Identify the blood parasite species.
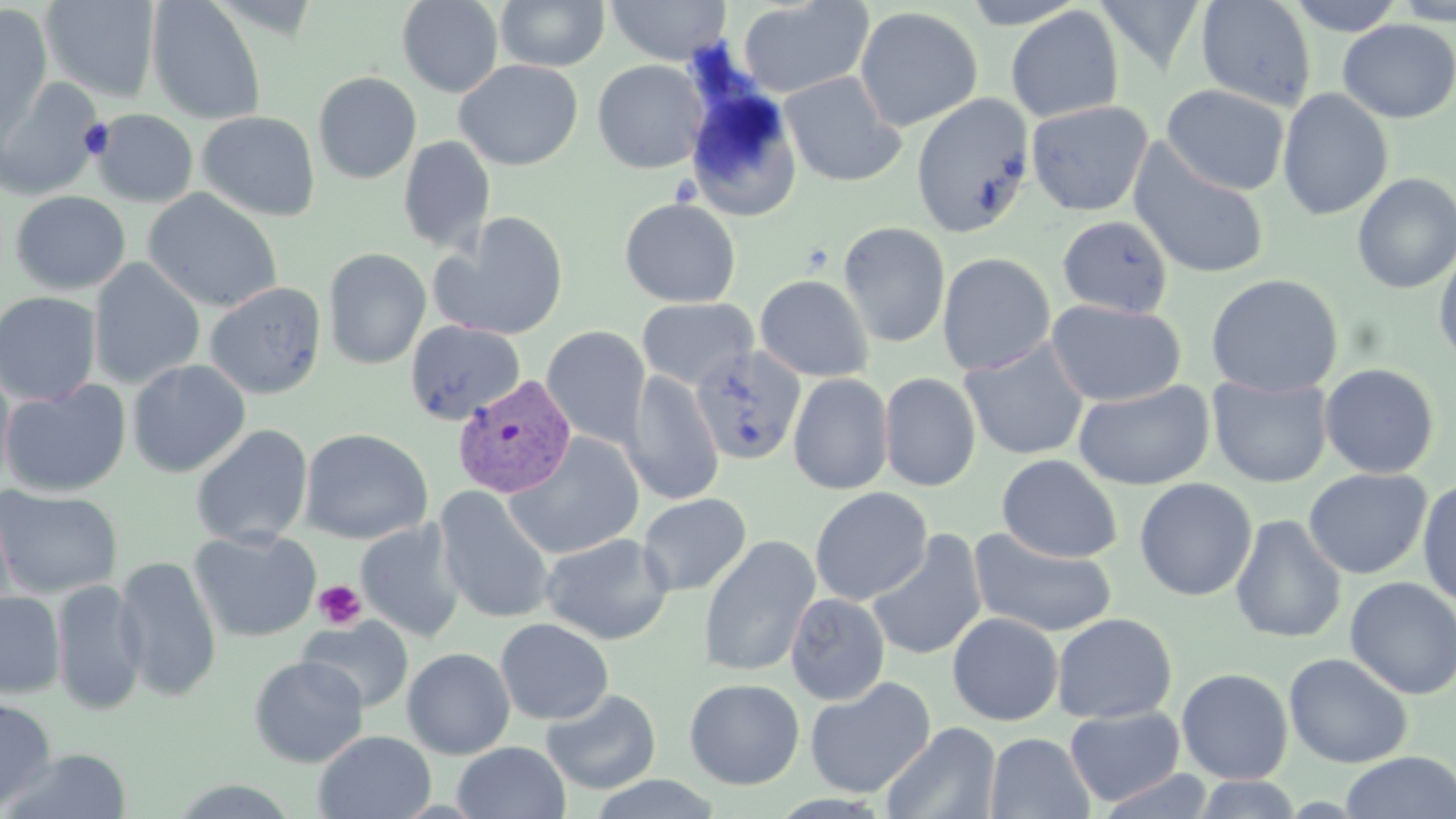

Plasmodium vivax.

preparation = thin blood smear
image size = 1456×819 pixels
uninfected red blood cell locations = approximate bounding boxes as (x1, y1, x2, y2) in pixels: (40, 0, 161, 103), (397, 0, 504, 97), (495, 0, 610, 71), (605, 0, 732, 65), (737, 0, 874, 99), (958, 0, 1088, 28), (1093, 0, 1207, 77), (1195, 0, 1317, 112), (1284, 0, 1407, 36), (1390, 0, 1456, 25), (147, 1, 266, 125), (0, 4, 53, 139), (1006, 5, 1124, 123), (854, 6, 984, 132), (1337, 19, 1456, 123), (454, 59, 583, 171), (592, 59, 708, 173), (313, 71, 422, 184), (778, 71, 907, 188), (0, 77, 104, 201), (1162, 84, 1291, 196), (1277, 88, 1394, 221), (685, 89, 803, 222), (911, 94, 1035, 238), (1026, 100, 1154, 217), (90, 109, 198, 207), (197, 111, 321, 221), (398, 136, 496, 255), (1128, 141, 1271, 280), (1352, 172, 1456, 295), (142, 188, 283, 313), (10, 191, 130, 295), (619, 198, 741, 308), (432, 212, 571, 342), (1057, 215, 1173, 318), (838, 221, 951, 348), (1433, 242, 1456, 372), (323, 248, 431, 370), (937, 252, 1056, 376), (88, 259, 205, 389), (1205, 273, 1343, 396), (754, 274, 874, 382), (204, 282, 327, 398), (0, 291, 102, 407), (637, 297, 758, 390), (1045, 299, 1186, 407), (405, 320, 525, 425), (541, 326, 651, 448), (959, 338, 1090, 462), (127, 359, 250, 478), (0, 362, 15, 489), (1319, 363, 1440, 479), (623, 372, 724, 506), (878, 372, 981, 492), (788, 373, 894, 495), (1207, 374, 1332, 488), (0, 380, 131, 498), (1073, 380, 1214, 491), (191, 424, 313, 548), (299, 428, 432, 544), (503, 433, 644, 560), (996, 454, 1122, 563), (1303, 468, 1432, 579), (1417, 476, 1456, 608), (1134, 478, 1257, 601), (0, 486, 122, 598), (434, 486, 556, 624), (810, 487, 932, 605), (638, 493, 752, 597), (1230, 514, 1347, 644), (356, 520, 466, 642), (188, 528, 322, 643), (968, 529, 1118, 638), (865, 530, 988, 663), (539, 532, 674, 645), (697, 535, 820, 677), (113, 556, 222, 702), (1344, 577, 1456, 700), (52, 578, 147, 716), (0, 592, 65, 698), (785, 592, 890, 705), (947, 612, 1064, 726), (1051, 613, 1177, 724), (297, 616, 414, 713), (495, 618, 614, 725), (402, 647, 516, 760), (1283, 652, 1414, 769), (248, 655, 369, 767), (1176, 667, 1294, 784), (804, 677, 936, 798), (684, 678, 804, 790), (540, 687, 662, 795), (0, 696, 56, 811), (1064, 706, 1185, 807), (881, 722, 1001, 819), (314, 731, 436, 818), (985, 732, 1095, 819), (452, 741, 571, 819), (1, 747, 134, 819), (1339, 751, 1456, 819), (1094, 769, 1217, 818), (586, 774, 726, 818), (1190, 775, 1305, 818)
modality = light microscopy
Plasmodium vivax-infected red blood cell locations = approximate bounding boxes as (x1, y1, x2, y2) in pixels: (690, 344, 807, 467), (452, 374, 576, 499)
field of view = single
stain = May-Grünwald-Giemsa
platelet locations = approximate bounding boxes as (x1, y1, x2, y2) in pixels: (313, 579, 367, 630)
magnification = 1000x